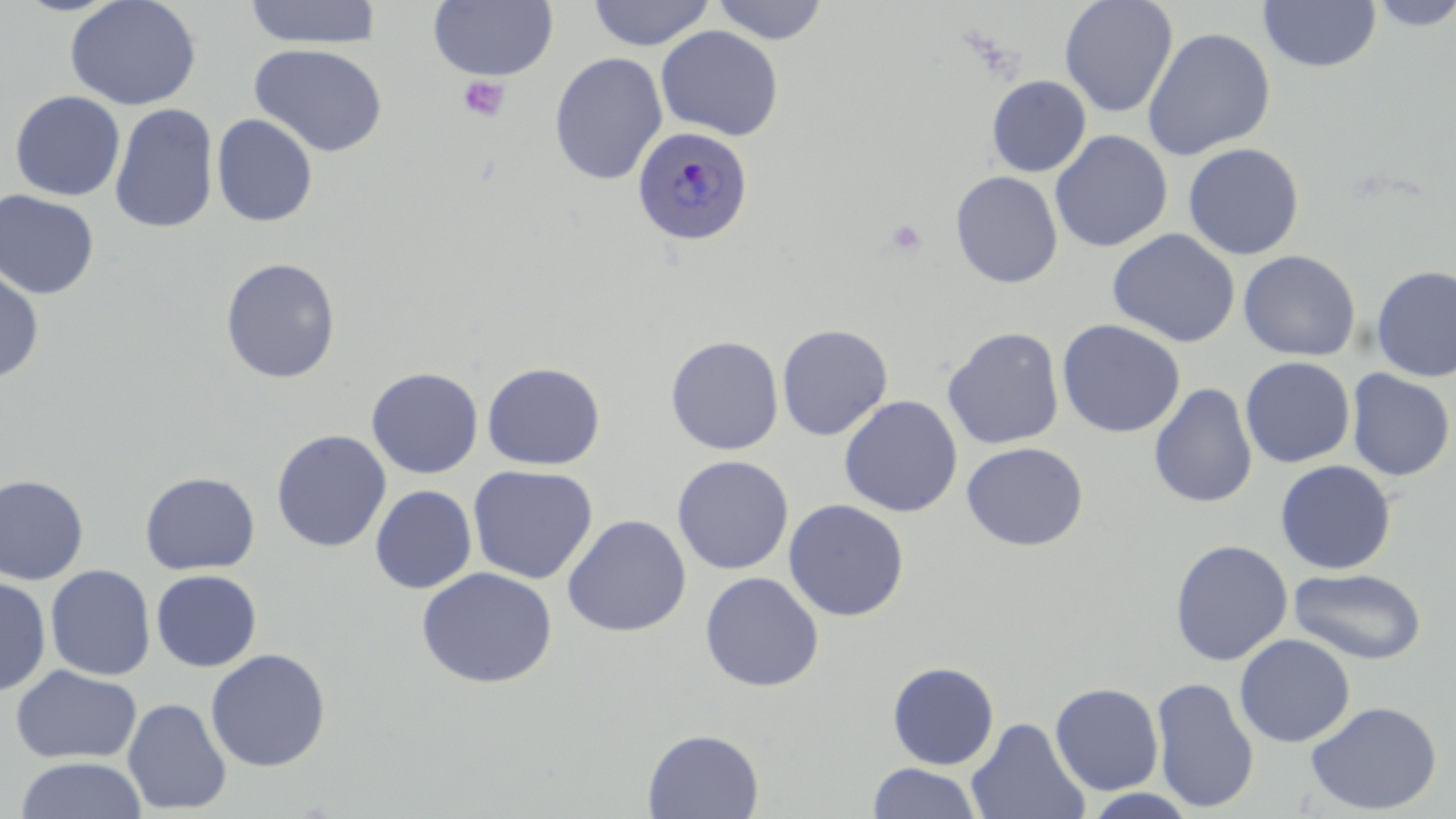
Summary:
  - Coordinate format: approximate bounding boxes as named x1/y1/x2/y2 corners in pixels
  - Platelet locations: (x1=458, y1=75, x2=510, y2=122), (x1=884, y1=219, x2=927, y2=257)
  - Uninfected red blood cell locations: (x1=64, y1=0, x2=202, y2=111), (x1=244, y1=0, x2=381, y2=49), (x1=429, y1=0, x2=558, y2=81), (x1=586, y1=0, x2=716, y2=50), (x1=710, y1=0, x2=830, y2=45), (x1=1059, y1=0, x2=1178, y2=118), (x1=1258, y1=0, x2=1381, y2=74), (x1=1365, y1=0, x2=1456, y2=30), (x1=656, y1=25, x2=784, y2=141), (x1=1142, y1=27, x2=1275, y2=161), (x1=249, y1=43, x2=388, y2=157), (x1=549, y1=52, x2=668, y2=185), (x1=987, y1=75, x2=1091, y2=176), (x1=9, y1=90, x2=126, y2=201), (x1=109, y1=103, x2=219, y2=234), (x1=211, y1=113, x2=318, y2=227), (x1=1050, y1=130, x2=1173, y2=253), (x1=1183, y1=143, x2=1305, y2=260), (x1=950, y1=170, x2=1063, y2=288), (x1=0, y1=189, x2=100, y2=300), (x1=1107, y1=228, x2=1240, y2=348), (x1=1238, y1=250, x2=1361, y2=361), (x1=220, y1=257, x2=341, y2=384), (x1=1371, y1=264, x2=1456, y2=382), (x1=0, y1=265, x2=44, y2=382), (x1=1057, y1=319, x2=1186, y2=438), (x1=776, y1=324, x2=893, y2=441), (x1=942, y1=327, x2=1065, y2=450), (x1=665, y1=335, x2=784, y2=455), (x1=1240, y1=356, x2=1355, y2=468), (x1=482, y1=362, x2=605, y2=470), (x1=366, y1=367, x2=483, y2=479), (x1=1346, y1=369, x2=1455, y2=481), (x1=1149, y1=383, x2=1258, y2=508), (x1=839, y1=395, x2=963, y2=517), (x1=271, y1=429, x2=392, y2=552), (x1=961, y1=441, x2=1088, y2=551), (x1=671, y1=455, x2=794, y2=575), (x1=1275, y1=460, x2=1396, y2=575), (x1=467, y1=465, x2=598, y2=584), (x1=139, y1=470, x2=260, y2=575), (x1=0, y1=474, x2=89, y2=584), (x1=370, y1=485, x2=477, y2=594), (x1=783, y1=499, x2=909, y2=621), (x1=562, y1=514, x2=691, y2=637), (x1=1169, y1=539, x2=1293, y2=666), (x1=45, y1=564, x2=156, y2=681), (x1=416, y1=567, x2=558, y2=689), (x1=1289, y1=568, x2=1427, y2=665), (x1=150, y1=569, x2=261, y2=671), (x1=700, y1=571, x2=824, y2=692), (x1=0, y1=575, x2=51, y2=696), (x1=1234, y1=634, x2=1356, y2=747), (x1=205, y1=648, x2=331, y2=772), (x1=887, y1=661, x2=1000, y2=769), (x1=10, y1=665, x2=142, y2=765), (x1=1151, y1=675, x2=1260, y2=813), (x1=1050, y1=682, x2=1164, y2=795), (x1=122, y1=698, x2=232, y2=815), (x1=1306, y1=700, x2=1442, y2=815), (x1=966, y1=716, x2=1090, y2=819), (x1=642, y1=728, x2=764, y2=818), (x1=13, y1=757, x2=147, y2=819), (x1=867, y1=763, x2=983, y2=819), (x1=1081, y1=788, x2=1198, y2=818)
  - Plasmodium ovale-infected red blood cell locations: (x1=632, y1=125, x2=753, y2=246)
  - Slide-level diagnosis: Plasmodium ovale
  - Image size: 1456×819 pixels
  - Stain: May-Grünwald-Giemsa
  - Field of view: single
  - Magnification: 1000x
  - Modality: optical microscopy
  - Preparation: thin blood film